State the preparation type.
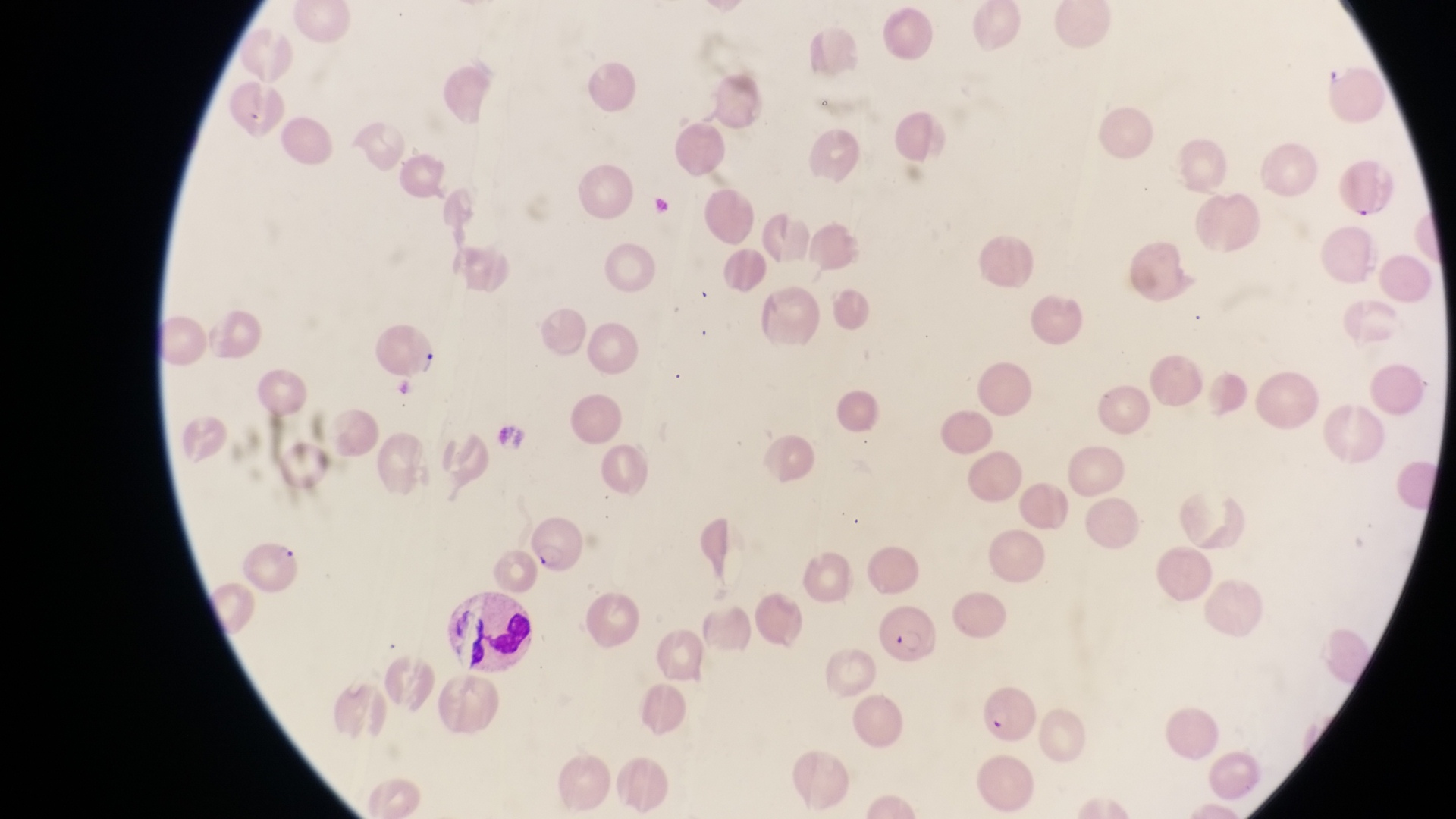

This is a thin smear.

Approximate bounding boxes as (left, top, right, bottom) in pixels. Parasitised red blood cell locations: (372, 322, 436, 380), (529, 512, 588, 578), (240, 534, 304, 597), (877, 601, 943, 665), (977, 684, 1038, 739). Leukocyte locations: (444, 587, 536, 661). One field of view. Image is 1456×819 pixels. Magnification of 1000x. Captured by a smartphone held over the eyepiece of an Olympus CX-23 microscope. Sample from Uganda.